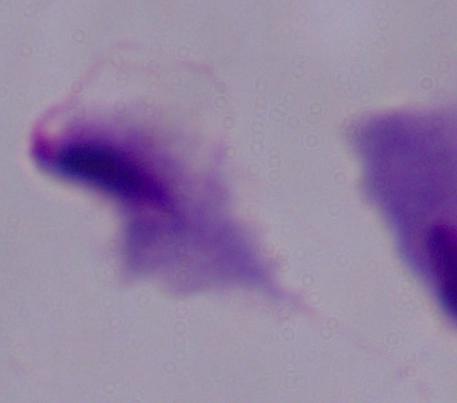
Summary:
  - Modality: photomicrograph
  - Identification: trichomonad
  - Magnification: 1000x